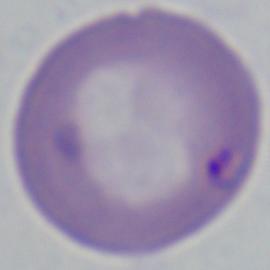

identification = Babesia
magnification = 1000x
modality = micrograph